Locate every malaria parasite and every leukocyte.
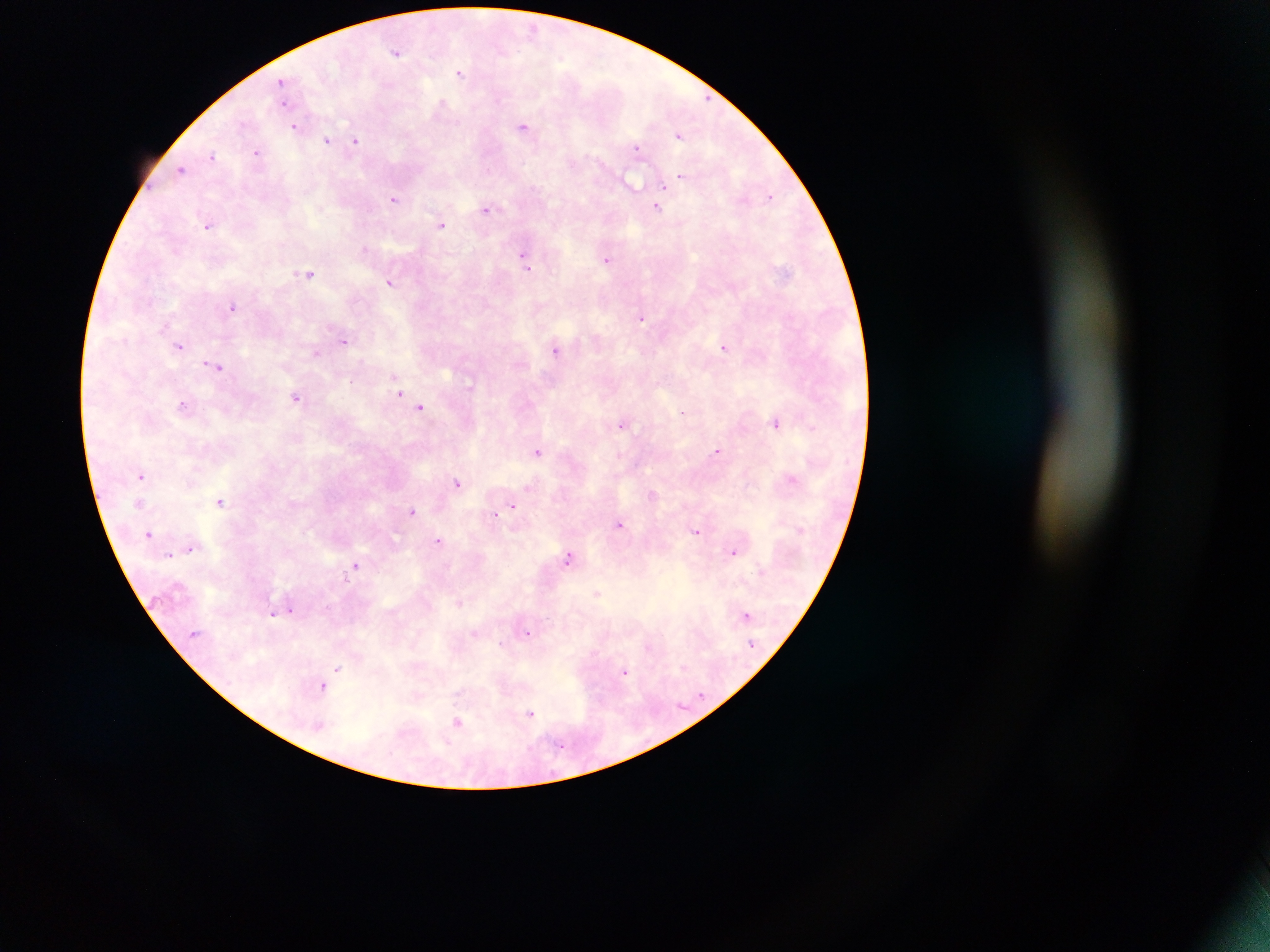
Approximate centers as {x, y} in pixels.
Malaria parasites: {533, 29}, {396, 51}, {460, 72}, {282, 81}, {283, 104}, {442, 104}, {294, 126}, {523, 126}, {679, 136}, {327, 140}, {355, 140}, {636, 147}, {257, 153}, {213, 156}, {182, 169}, {681, 177}, {632, 182}, {664, 186}, {770, 196}, {394, 199}, {657, 207}, {487, 210}, {442, 225}, {207, 227}, {364, 248}, {523, 254}, {608, 259}, {527, 268}, {309, 273}, {390, 282}, {232, 307}, {641, 317}, {164, 326}, {343, 340}, {180, 346}, {724, 347}, {555, 350}, {316, 352}, {216, 367}, {399, 392}, {296, 397}, {182, 405}, {421, 408}, {681, 413}, {776, 423}, {621, 425}, {813, 428}, {717, 450}, {538, 451}, {141, 476}, {791, 479}, {457, 482}, {529, 487}, {652, 494}, {220, 501}, {513, 506}, {412, 511}, {494, 515}, {619, 525}, {696, 530}, {149, 534}, {439, 540}, {190, 548}, {733, 552}, {169, 554}, {568, 557}, {356, 566}, {597, 592}, {459, 602}, {291, 610}, {273, 615}, {745, 615}, {528, 633}, {474, 634}, {648, 646}, {338, 669}, {625, 672}, {323, 687}, {530, 713}, {457, 723}.
No leukocytes observed.

field_of_view: single
preparation: thick blood film
image_size: 1270×952 pixels
capture: mobile-phone photograph through a microscope
country: Ghana